Locate and identify every blood parasite.
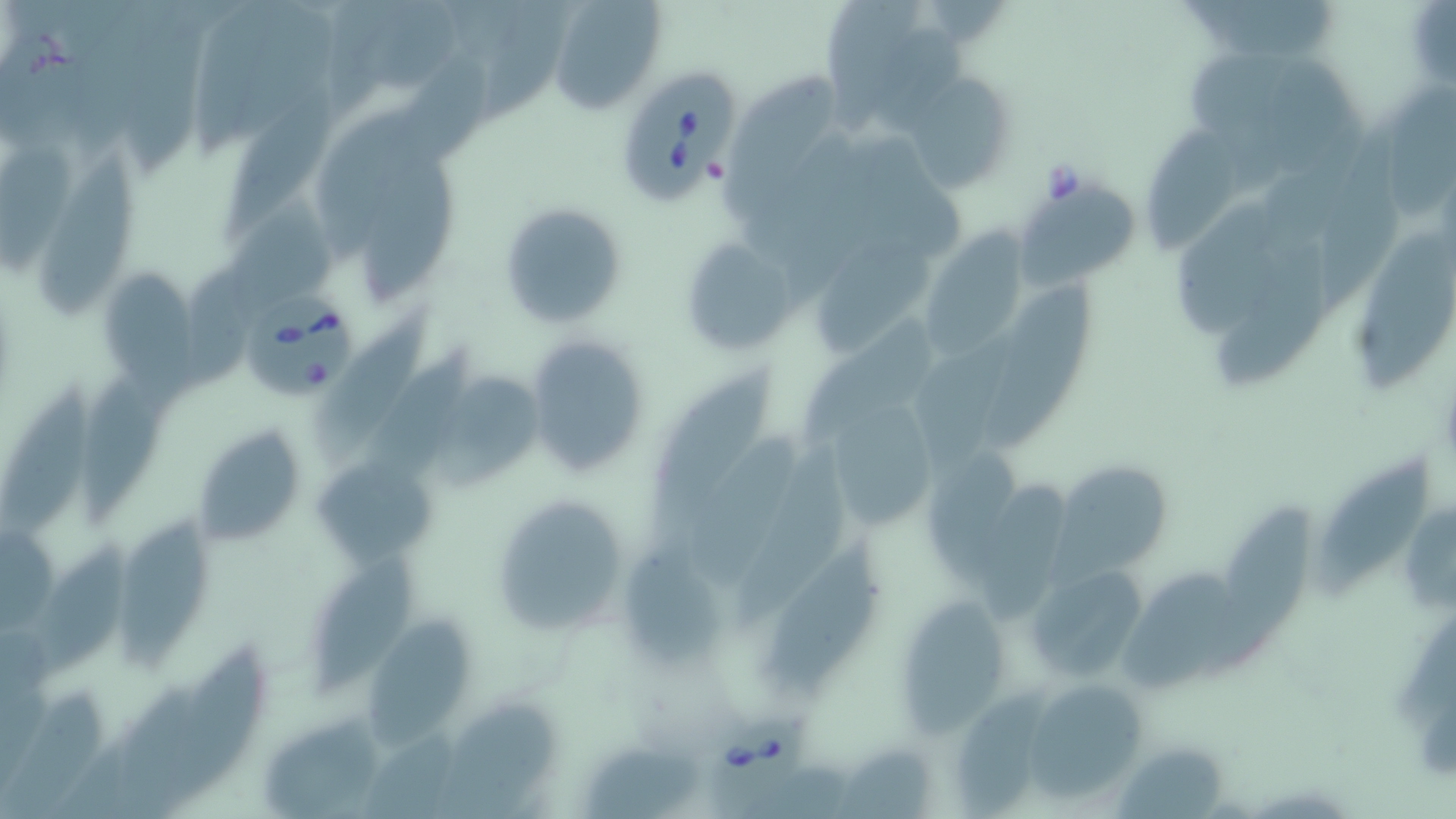

Approximate bounding boxes as [x1, y1, x2, y2] in pixels.
Babesia divergens-infected red blood cells: [624, 66, 742, 207], [242, 288, 358, 401], [705, 716, 808, 819].
No Plasmodium falciparum, Plasmodium ovale, Plasmodium malariae, Plasmodium vivax, or Trypanosoma brucei observed.

slide_level_diagnosis: Babesia divergens
image_size: 1456×819 pixels
uninfected_red_blood_cell_locations: 'approximate bounding boxes as [x1, y1, x2, y2] in pixels: [547, 0, 664, 113], [827, 0, 925, 138], [901, 71, 1018, 195], [224, 79, 343, 244], [1382, 82, 1455, 227], [1140, 129, 1241, 248], [0, 131, 84, 279], [31, 146, 135, 316], [351, 157, 465, 302], [1012, 189, 1140, 291], [500, 201, 627, 328], [1176, 208, 1280, 347], [918, 227, 1030, 362], [1358, 232, 1455, 394], [679, 237, 804, 357], [810, 240, 938, 361], [1217, 248, 1334, 394], [98, 267, 198, 380], [979, 276, 1101, 452], [316, 307, 437, 458], [914, 318, 1022, 467], [523, 332, 653, 480], [373, 344, 476, 484], [633, 363, 778, 547], [79, 370, 166, 534], [436, 371, 550, 488], [4, 373, 96, 535], [819, 398, 940, 532], [193, 425, 306, 551], [686, 430, 799, 586], [735, 444, 835, 623], [313, 457, 438, 565], [1321, 457, 1429, 597], [1043, 468, 1169, 594], [984, 480, 1070, 625], [489, 492, 634, 639], [1205, 505, 1317, 681], [118, 509, 214, 676], [761, 535, 886, 700], [29, 541, 133, 676], [627, 541, 728, 666], [311, 552, 421, 692], [1021, 562, 1148, 685], [1111, 568, 1237, 694], [900, 599, 1007, 739], [369, 617, 469, 744], [170, 645, 269, 802], [1026, 682, 1146, 804], [948, 686, 1060, 819], [0, 689, 110, 819], [438, 701, 559, 819], [257, 710, 386, 817], [582, 745, 700, 819], [839, 747, 938, 819], [1117, 748, 1223, 818]'
magnification: 1000x
modality: light microscopy
field_of_view: single
preparation: thin blood smear
stain: May-Grünwald-Giemsa